Describe the morphology of the erythrocytes.
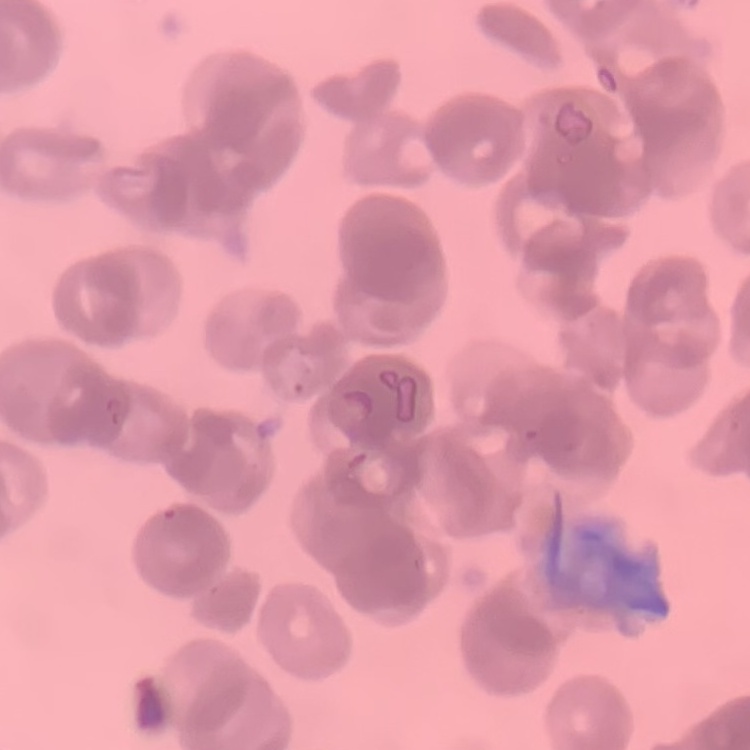

Rouleaux formation.

Square crop of a larger photomicrograph. Thin peripheral smear. Stained with either Field's or Giemsa.